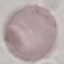

Summary:
  - Malaria status: uninfected
  - Image type: cell patch, automatically extracted from a larger field of view and resized to 64 × 64 pixels
  - Preparation: thin blood film
  - Capture: smartphone camera at the microscope eyepiece
  - Stain: Giemsa